Locate and identify every blood parasite.
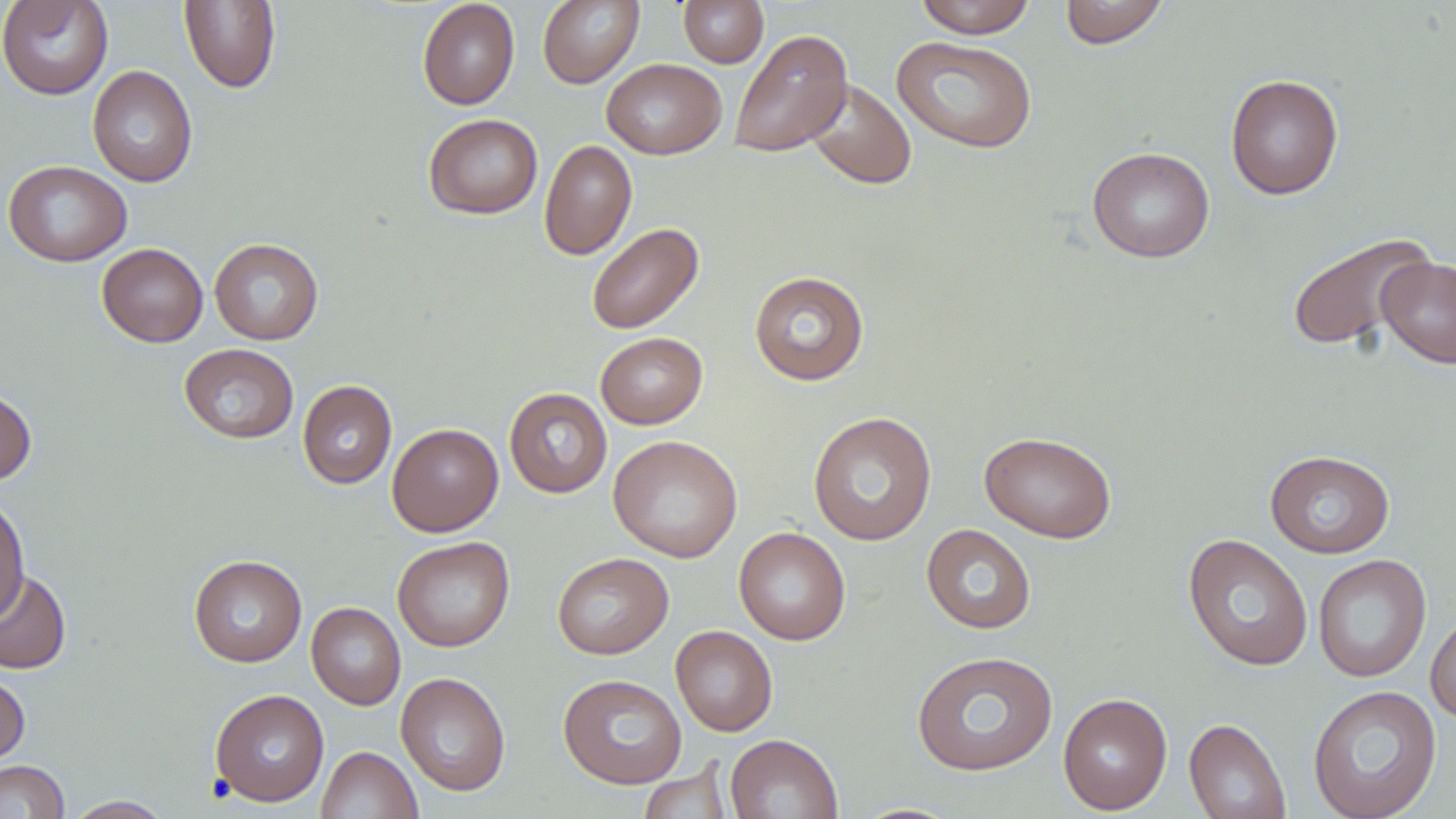

No blood parasites seen.

{
  "slide_level_diagnosis": "negative for blood parasites",
  "stain": "May-Grünwald-Giemsa",
  "magnification": "1000x",
  "field_of_view": "single",
  "uninfected_red_blood_cell_locations": "approximate bounding boxes as (x1,y1)-(x2,y2) corner pairs in pixels: (0,0)-(114,100), (417,0)-(519,110), (537,0)-(644,88), (678,0)-(768,68), (915,0)-(1036,38), (1059,0)-(1168,49), (179,1)-(280,93), (730,29)-(853,157), (891,36)-(1037,154), (601,58)-(727,159), (87,65)-(198,188), (1225,74)-(1344,200), (804,79)-(917,190), (423,113)-(543,219), (539,139)-(637,260), (1087,146)-(1215,263), (3,160)-(133,267), (586,222)-(704,334), (1286,232)-(1437,353), (209,238)-(323,345), (97,243)-(208,347), (1376,256)-(1456,369), (749,270)-(869,386), (595,332)-(707,429), (178,343)-(299,444), (297,380)-(397,489), (0,388)-(36,486), (504,388)-(612,498), (808,412)-(937,546), (387,423)-(503,536), (979,431)-(1117,543), (608,435)-(743,563), (1265,449)-(1395,558), (0,495)-(30,623), (922,524)-(1036,634), (733,526)-(851,645), (1183,533)-(1313,672), (392,536)-(514,652), (552,552)-(673,659), (1313,553)-(1432,683), (188,554)-(307,667), (0,569)-(71,675), (306,602)-(405,710), (1426,610)-(1456,724), (671,625)-(778,736), (912,650)-(1058,777), (0,671)-(30,766), (395,672)-(511,796), (558,673)-(687,789), (1307,684)-(1442,819), (209,688)-(329,807), (1058,692)-(1173,815), (1184,717)-(1291,819), (725,733)-(843,819), (316,746)-(423,819), (0,760)-(69,818), (637,761)-(735,819), (62,796)-(173,818)",
  "modality": "optical microscopy",
  "preparation": "thin blood smear",
  "image_size": "1456×819 pixels"
}